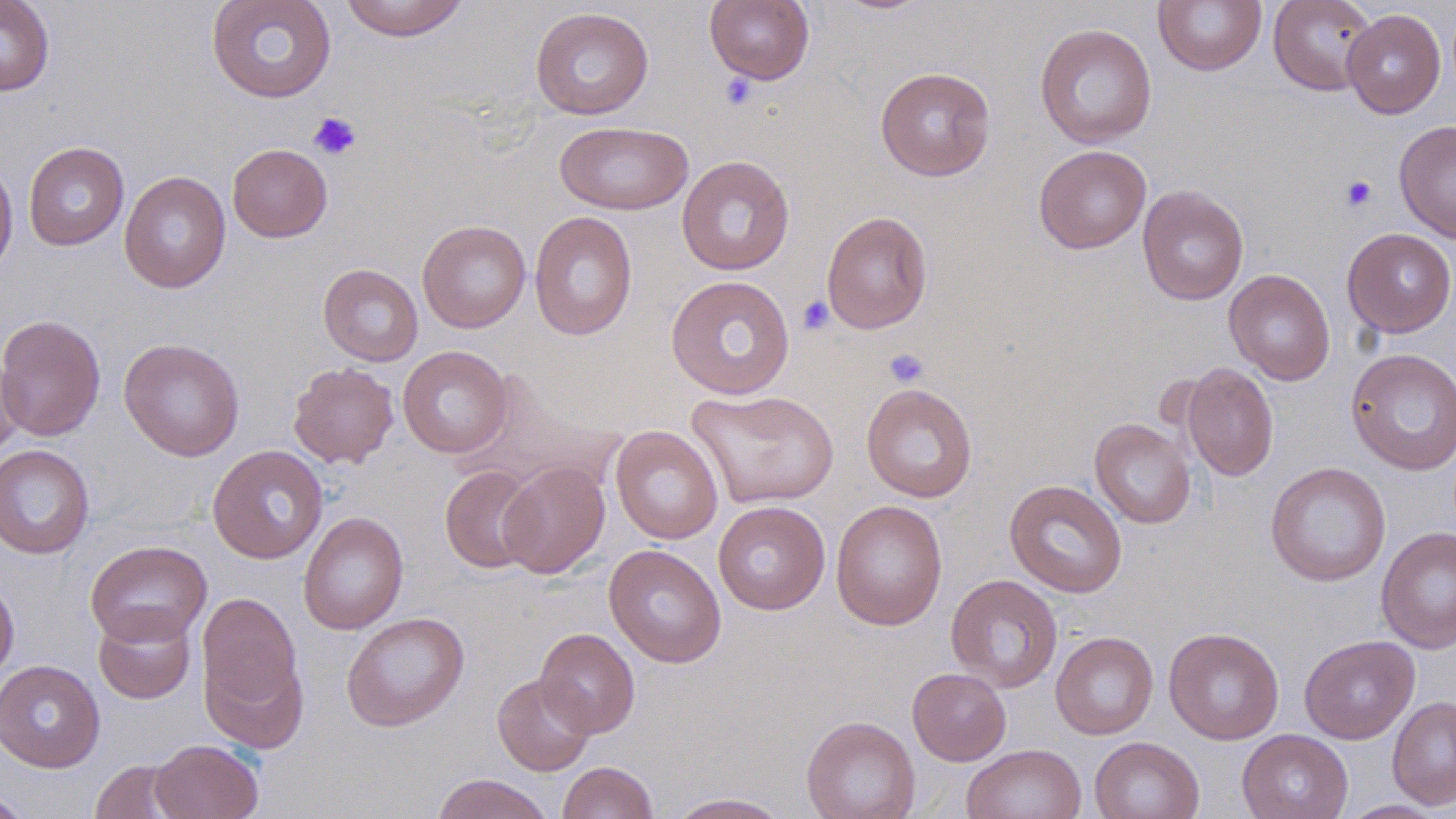

Approximate bounding boxes as [x1, y1, x2, y2] in pixels. Platelet locations: [720, 73, 758, 110], [308, 112, 362, 161], [1340, 174, 1378, 213], [797, 295, 835, 335], [884, 348, 929, 388]. Uninfected red blood cell locations: [0, 0, 55, 96], [206, 0, 336, 103], [339, 0, 469, 41], [704, 0, 815, 86], [1153, 0, 1266, 75], [1268, 0, 1378, 96], [530, 7, 654, 120], [1342, 9, 1445, 118], [1034, 23, 1157, 148], [875, 66, 996, 181], [1394, 119, 1456, 243], [554, 120, 693, 215], [23, 141, 130, 251], [227, 143, 332, 243], [1033, 144, 1151, 254], [676, 155, 795, 276], [0, 158, 18, 280], [118, 171, 231, 294], [1137, 185, 1249, 305], [821, 210, 934, 334], [529, 211, 638, 341], [417, 219, 531, 333], [1342, 228, 1456, 337], [318, 263, 423, 366], [1224, 269, 1336, 385], [665, 275, 795, 399], [0, 314, 106, 441], [118, 337, 245, 461], [397, 345, 512, 458], [0, 347, 25, 461], [1345, 348, 1456, 475], [288, 362, 399, 468], [1181, 363, 1278, 481], [464, 371, 625, 492], [861, 383, 978, 503], [685, 388, 840, 509], [1090, 418, 1196, 529], [610, 425, 722, 544], [0, 444, 94, 559], [207, 445, 328, 564], [498, 461, 609, 578], [1265, 461, 1391, 586], [439, 465, 541, 573], [1004, 479, 1128, 597], [831, 499, 948, 631], [713, 501, 830, 615], [298, 511, 409, 635], [1376, 526, 1456, 654], [85, 540, 212, 647], [604, 544, 727, 668], [945, 574, 1063, 693], [0, 576, 19, 682], [196, 591, 304, 723], [93, 607, 197, 704], [341, 612, 470, 732], [1163, 626, 1284, 744], [534, 628, 640, 737], [1051, 631, 1158, 740], [1299, 635, 1420, 744], [204, 649, 309, 754], [1, 659, 105, 772], [907, 667, 1011, 765], [492, 673, 595, 776], [1386, 696, 1456, 810], [801, 715, 920, 819], [1237, 729, 1354, 819], [1089, 736, 1204, 819], [151, 739, 263, 819], [961, 743, 1087, 819], [90, 760, 189, 819], [557, 761, 658, 819], [431, 773, 554, 819], [0, 789, 35, 819], [668, 792, 791, 818], [1338, 800, 1447, 818]. Slide-level diagnosis: no evidence of blood parasites. Thin blood smear. 1000x magnification. One field of a larger specimen. Image is 1456×819 pixels. Light microscopy. May-Grünwald-Giemsa-stained preparation.